Outline each Babesia divergens-infected red blood cell.
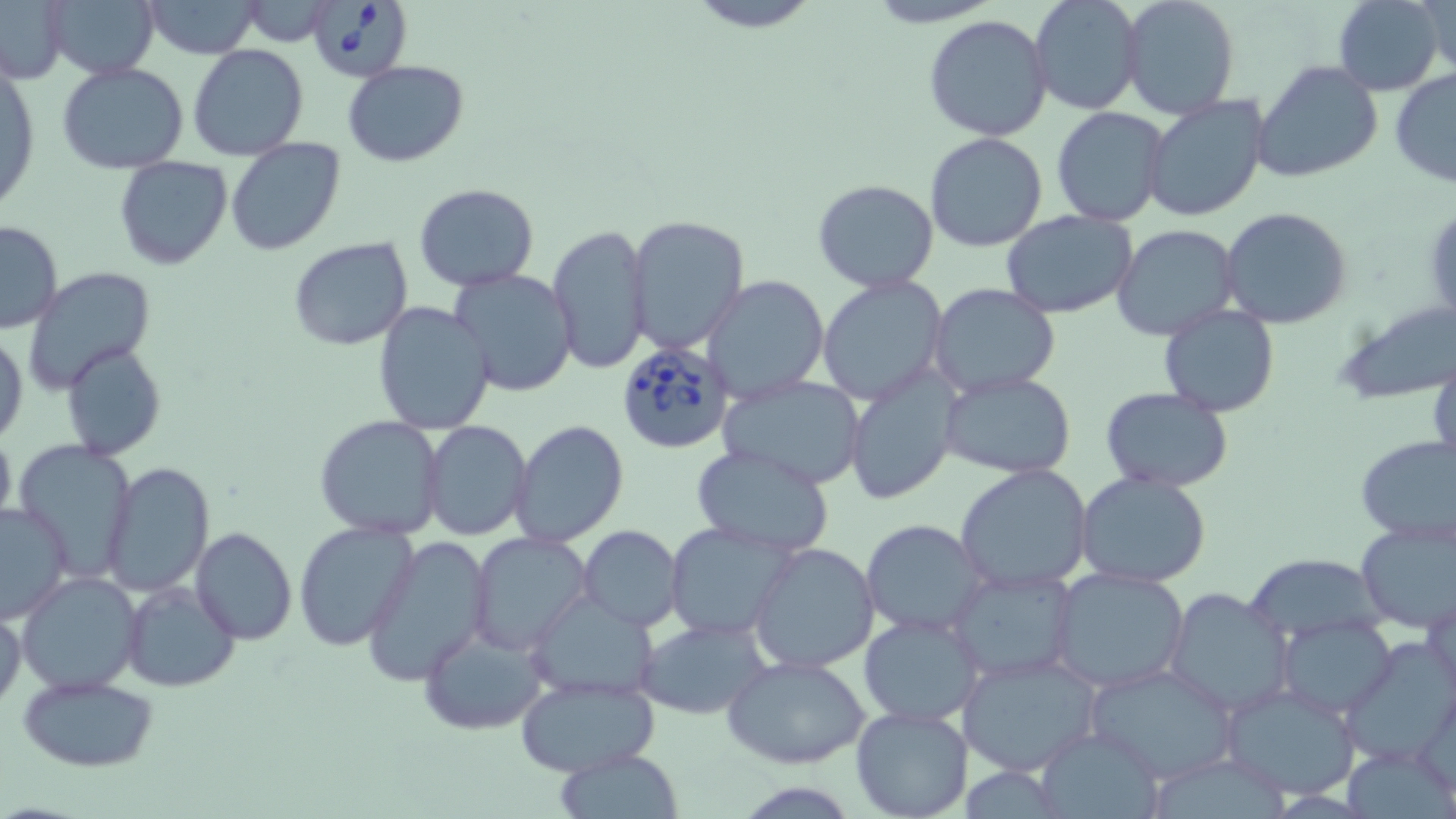

Approximate bounding boxes as [x1, y1, x2, y2] in pixels.
Babesia divergens-infected red blood cells: [315, 0, 410, 81], [615, 337, 737, 454].

Summary:
  - Uninfected red blood cell locations: [43, 0, 160, 80], [137, 0, 265, 57], [1030, 0, 1143, 116], [1332, 0, 1446, 97], [1414, 0, 1456, 77], [1119, 1, 1239, 120], [0, 2, 69, 83], [238, 2, 336, 47], [677, 2, 830, 33], [923, 14, 1054, 140], [188, 45, 309, 162], [343, 60, 470, 166], [1254, 60, 1384, 183], [1, 62, 39, 218], [57, 63, 189, 175], [1389, 69, 1456, 190], [1141, 95, 1269, 223], [1051, 106, 1172, 227], [924, 131, 1049, 252], [226, 139, 344, 255], [114, 157, 234, 271], [812, 178, 942, 293], [413, 183, 541, 292], [1221, 206, 1354, 330], [1000, 210, 1138, 319], [624, 214, 750, 355], [0, 220, 63, 334], [548, 223, 651, 375], [1112, 224, 1241, 341], [288, 236, 414, 351], [25, 268, 156, 395], [448, 268, 578, 395], [703, 275, 830, 401], [816, 276, 950, 407], [928, 284, 1061, 399], [371, 299, 495, 436], [1333, 300, 1455, 405], [1158, 305, 1280, 417], [1, 329, 26, 445], [62, 341, 166, 460], [1427, 351, 1456, 479], [845, 366, 960, 505], [938, 371, 1079, 477], [717, 376, 868, 490], [1101, 386, 1235, 493], [315, 415, 447, 539], [422, 419, 533, 541], [512, 419, 629, 549], [0, 421, 17, 540], [1354, 435, 1456, 549], [13, 439, 139, 577], [690, 444, 836, 557], [103, 463, 215, 595], [954, 464, 1096, 592], [1074, 472, 1212, 589], [0, 503, 72, 624], [1354, 518, 1456, 632], [860, 519, 988, 638], [293, 521, 416, 650], [665, 522, 798, 640], [579, 526, 684, 631], [189, 527, 297, 645], [468, 532, 592, 653], [361, 537, 492, 685], [748, 540, 881, 673], [1241, 552, 1389, 647], [946, 566, 1078, 683], [1048, 567, 1192, 694], [17, 571, 143, 695], [121, 581, 238, 693], [1164, 587, 1293, 716], [1425, 589, 1456, 709], [524, 590, 662, 700], [0, 607, 26, 711], [858, 613, 986, 728], [1278, 617, 1395, 717], [637, 619, 769, 718], [418, 625, 550, 734], [1343, 635, 1455, 766], [954, 650, 1105, 776], [722, 655, 873, 769], [1083, 663, 1242, 784], [513, 673, 663, 776], [18, 675, 160, 771], [1221, 685, 1363, 799], [850, 705, 974, 819], [1033, 725, 1167, 818], [552, 749, 686, 818]
  - Slide-level diagnosis: Babesia divergens
  - Preparation: thin blood film
  - Image size: 1456×819 pixels
  - Magnification: 1000x
  - Field of view: single
  - Modality: optical microscopy
  - Stain: May-Grünwald-Giemsa